Locate every Plasmodium parasite.
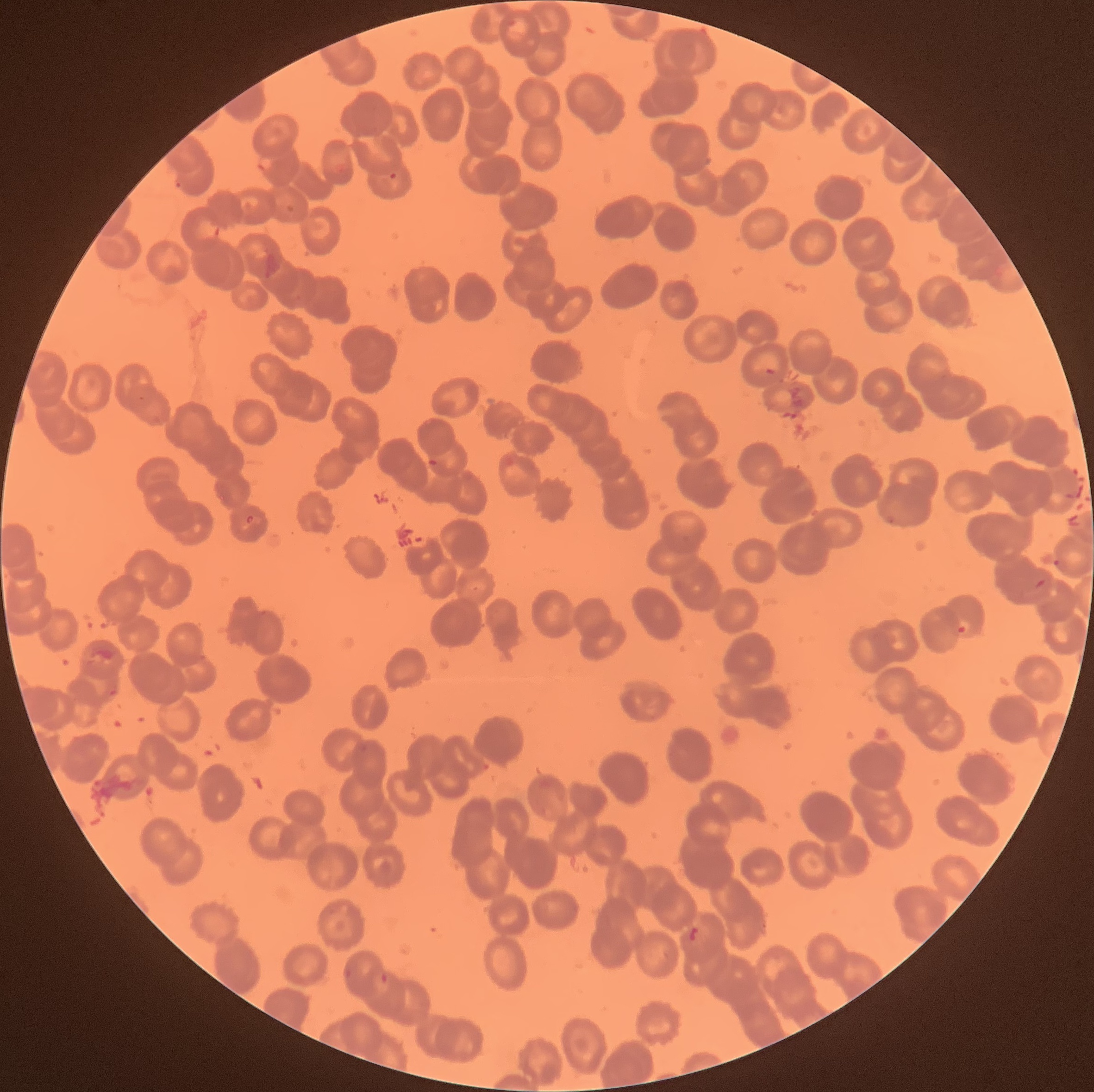

Approximate bounding boxes as (x1, y1, x2, y2) in pixels.
Plasmodium parasites: (388, 172, 399, 181), (173, 179, 186, 190), (425, 458, 437, 468), (1052, 557, 1063, 569), (1034, 578, 1048, 589), (957, 617, 971, 634), (379, 972, 389, 984).

modality = light microscopy
image size = 1094×1092 pixels
red blood cell morphology = rouleaux formation
preparation = thin blood film